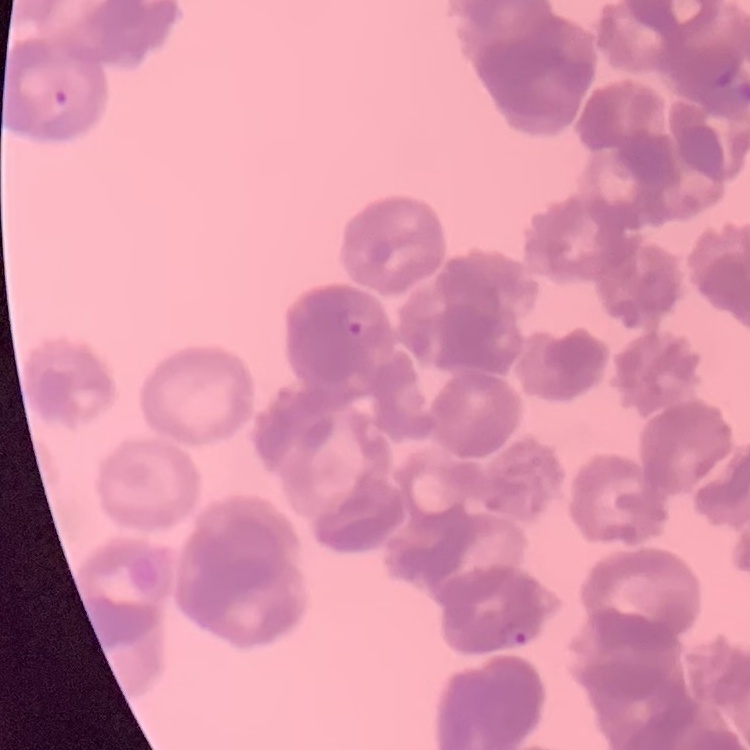
red_blood_cell_morphology: rouleaux formation
preparation: thin blood film
image_type: square crop of a larger photomicrograph
stain: Field's or Giemsa